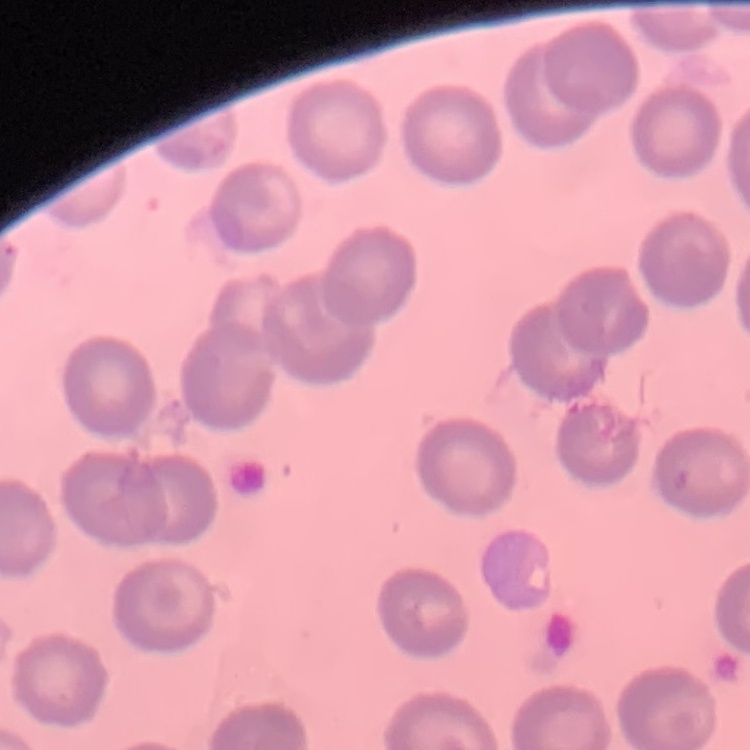 The erythrocytes show no rouleaux formation. Stained with either Field's or Giemsa. Thin blood film. One tile cut from a larger photomicrograph.